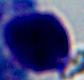
Summary:
  - Magnification: 1000x
  - Modality: photomicrograph
  - Identification: white blood cell